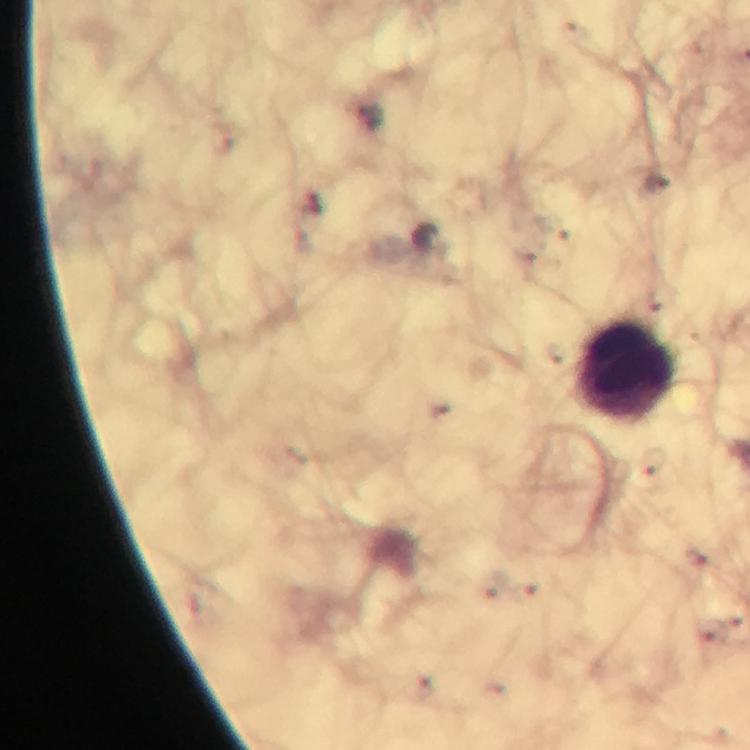

Approximate centers as [x, y] in pixels.
Summary:
  - Leukocyte locations: [625, 370]
  - Stain: Giemsa
  - Preparation: thick blood film
  - Immersion oil: applied
  - Plasmodium parasites: none detected
  - Cropped from: a single field of view
  - Context: from a malaria diagnostic workup
  - Capture: smartphone camera through the microscope
  - Image size: 750×750 pixels
  - Magnification: 100x